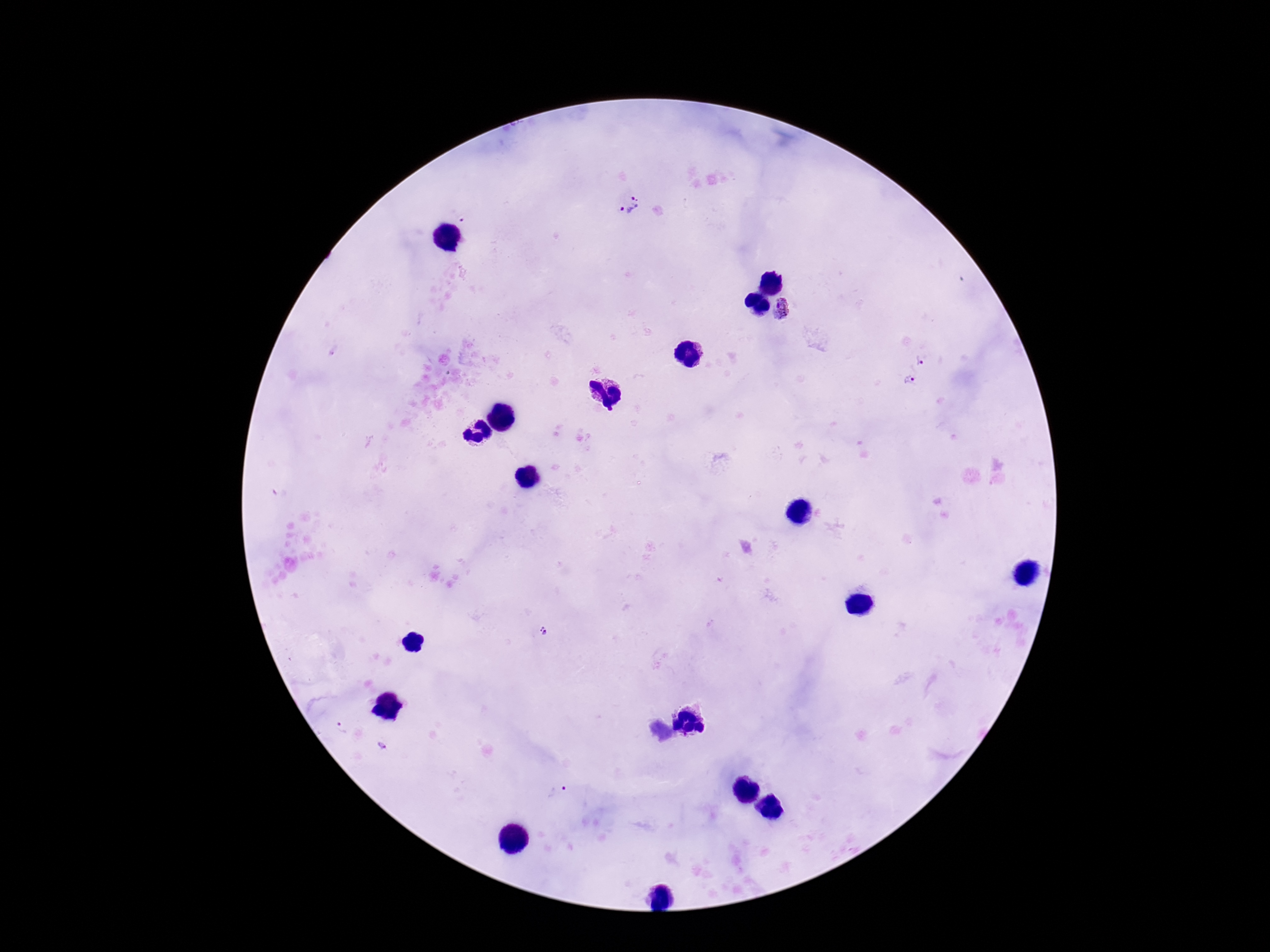

Approximate centers as (x, y) in pixels.
Summary:
  - Plasmodium parasite locations: (626, 205), (787, 309), (921, 358), (910, 379), (544, 631), (382, 745), (558, 791)
  - Image size: 1270×952 pixels
  - Patient malaria status: infected
  - Field of view: one from this slide
  - Magnification: 100x
  - Capture: smartphone camera through the microscope eyepiece
  - Preparation: thick blood film
  - Stain: Giemsa